Assess the morphology of the red blood cells.
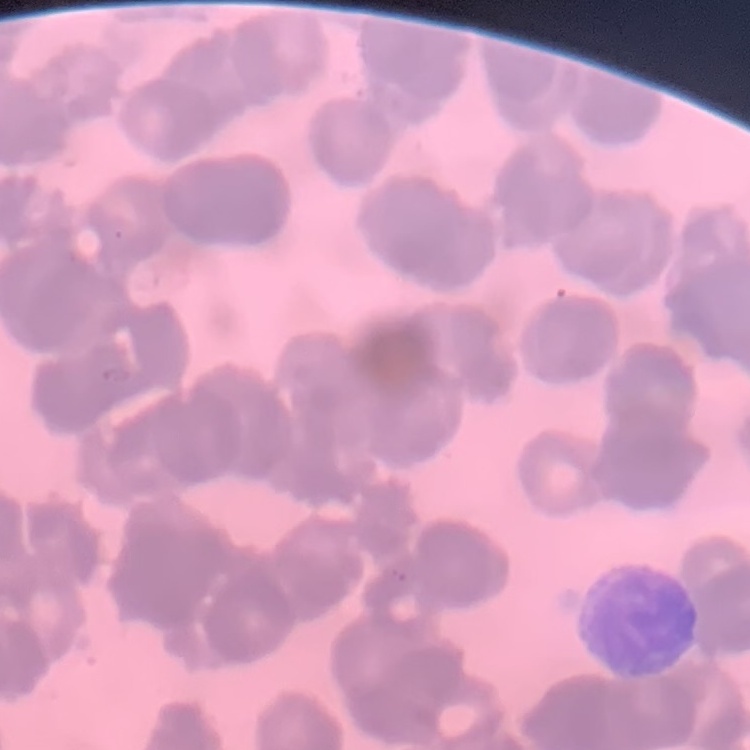
They show rouleaux formation.

Summary:
  - Stain: Field's or Giemsa
  - Preparation: thin blood film
  - Image type: square crop of a larger photomicrograph